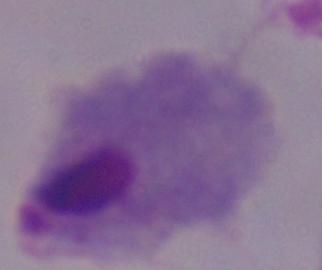

Summary:
  - Modality: photomicrograph
  - Identification: trichomonad
  - Magnification: 1000x